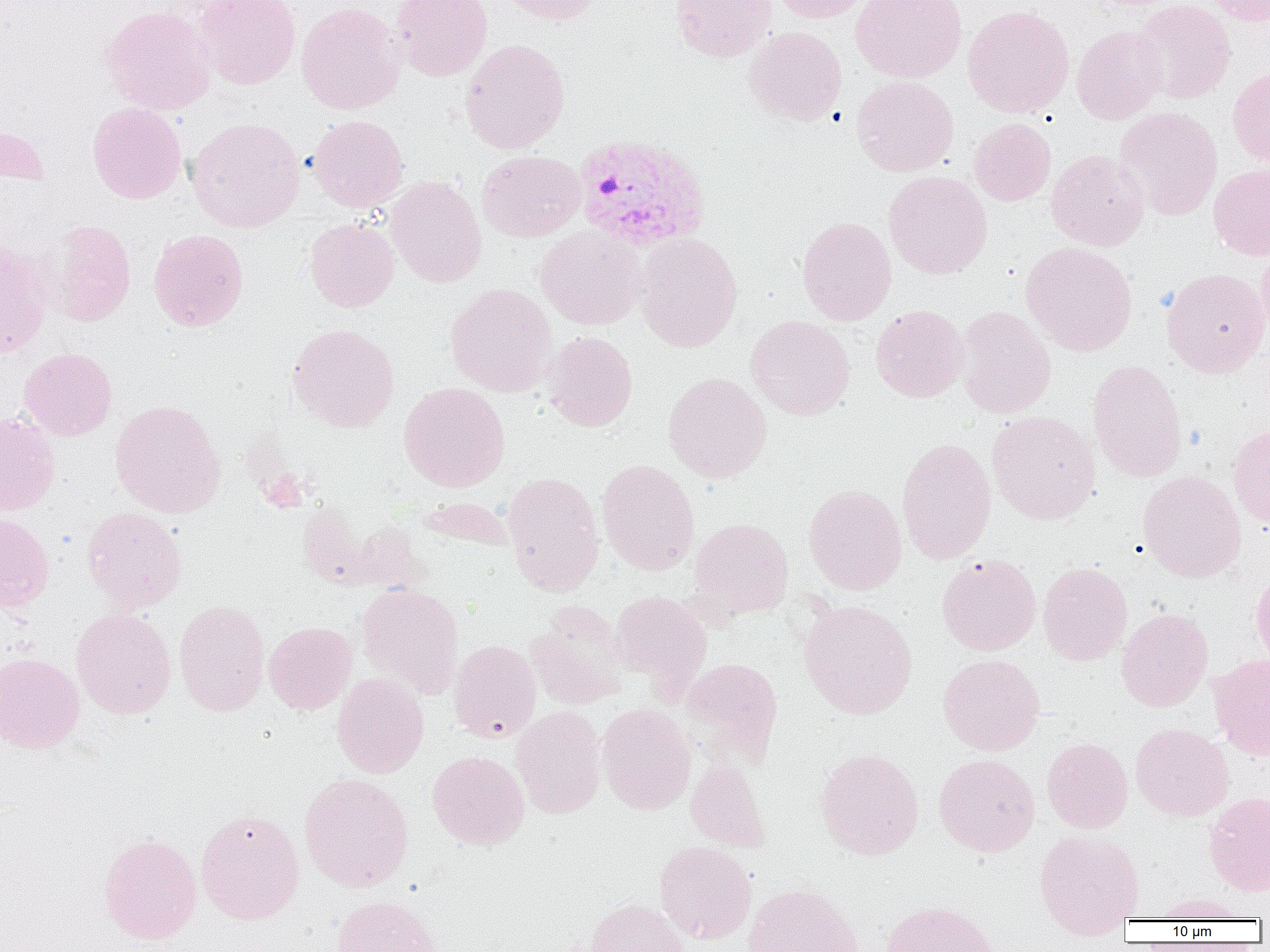
slide-level diagnosis = Plasmodium vivax
uninfected red blood cell locations = approximate bounding boxes as (x1,y1)-(x2,y2) corner pairs in pixels: (194,0)-(301,90), (391,0)-(492,81), (496,0)-(604,25), (670,0)-(776,62), (768,0)-(873,24), (851,0)-(967,83), (1132,0)-(1236,104), (1204,0)-(1270,27), (296,2)-(405,115), (101,5)-(216,115), (963,5)-(1074,118), (1071,24)-(1168,124), (745,26)-(847,126), (460,39)-(570,154), (1227,67)-(1270,166), (851,75)-(959,177), (87,102)-(187,203), (1115,106)-(1223,220), (307,115)-(409,212), (186,117)-(306,232), (969,118)-(1056,206), (0,122)-(50,188), (1046,149)-(1149,251), (476,150)-(585,242), (1209,164)-(1270,260), (883,170)-(992,279), (386,176)-(487,288), (797,216)-(897,325), (304,217)-(399,312), (46,220)-(136,326), (535,226)-(646,330), (149,229)-(248,331), (634,232)-(742,352), (0,237)-(52,359), (1020,241)-(1137,356), (1257,242)-(1270,340), (1161,267)-(1270,377), (445,282)-(558,396), (870,304)-(969,403), (956,305)-(1057,419), (745,315)-(855,420), (288,323)-(399,432), (541,331)-(638,431), (19,347)-(117,441), (1087,360)-(1187,483), (662,372)-(771,482), (399,382)-(510,491), (110,400)-(226,518), (987,411)-(1100,524), (0,412)-(61,516), (1228,423)-(1270,528), (896,437)-(997,564), (597,459)-(700,576), (502,470)-(604,596), (1138,470)-(1246,582), (803,484)-(907,595), (420,497)-(514,550), (82,506)-(187,612), (0,511)-(54,612), (689,517)-(794,618), (352,520)-(429,594), (936,553)-(1041,655), (1038,562)-(1133,665), (1251,569)-(1270,670), (357,582)-(463,697), (610,590)-(711,685), (174,599)-(270,716), (799,599)-(917,719), (526,601)-(629,709), (71,607)-(176,719), (1116,608)-(1213,712), (264,621)-(357,714), (449,639)-(541,743), (0,652)-(85,753), (937,653)-(1045,756), (1208,654)-(1270,760), (680,657)-(783,767), (332,672)-(429,778), (597,703)-(696,814), (511,706)-(606,819), (1130,723)-(1234,821), (1042,737)-(1133,833), (815,748)-(924,859), (427,749)-(530,849), (933,753)-(1040,857), (686,757)-(769,852), (299,772)-(414,892), (1204,791)-(1270,896), (195,808)-(304,924), (1034,830)-(1144,937), (98,833)-(202,944), (654,840)-(757,943), (742,883)-(864,952), (1149,892)-(1251,921), (330,894)-(442,952), (585,897)-(691,952), (881,900)-(1000,952)
image size = 1270×952 pixels
magnification = 1000x
Plasmodium vivax-infected red blood cell locations = approximate bounding boxes as (x1,y1)-(x2,y2) corner pairs in pixels: (573,133)-(711,252)
field of view = one of a larger specimen
modality = light microscopy
preparation = thin blood smear